Name the blood parasite species.
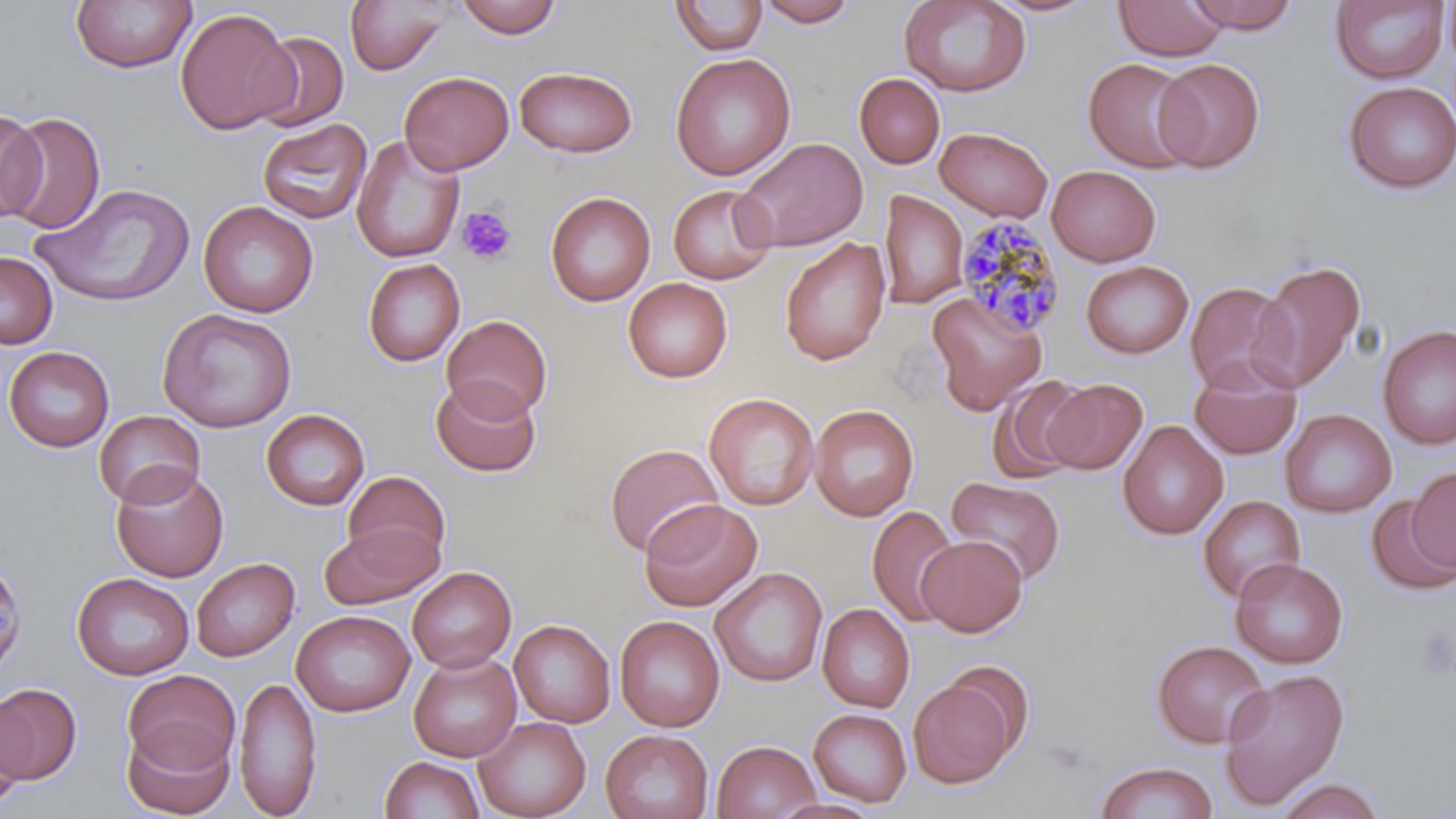

Plasmodium malariae.

preparation: thin blood film
uninfected_red_blood_cell_locations: 'approximate bounding boxes as [x1, y1, x2, y2] in pixels: [70, 0, 196, 74], [453, 0, 563, 39], [757, 0, 858, 27], [898, 0, 1032, 97], [987, 0, 1100, 17], [1184, 0, 1301, 33], [1443, 0, 1456, 68], [345, 1, 452, 76], [669, 1, 768, 56], [1113, 1, 1227, 61], [1329, 1, 1450, 85], [175, 8, 297, 135], [250, 31, 349, 132], [670, 52, 796, 181], [1082, 58, 1198, 173], [1153, 58, 1264, 173], [513, 65, 639, 157], [399, 70, 514, 174], [854, 74, 944, 168], [1342, 81, 1456, 194], [0, 110, 46, 223], [3, 111, 104, 234], [256, 117, 372, 224], [935, 127, 1053, 221], [350, 135, 466, 264], [734, 137, 869, 252], [1047, 165, 1161, 266], [32, 182, 194, 307], [667, 184, 776, 285], [879, 190, 968, 309], [544, 191, 656, 307], [198, 200, 319, 318], [779, 237, 891, 366], [0, 251, 58, 349], [1250, 258, 1367, 394], [362, 259, 465, 366], [1081, 260, 1194, 359], [623, 277, 733, 383], [1185, 281, 1295, 395], [927, 290, 1047, 414], [158, 307, 298, 432], [441, 314, 553, 422], [1377, 324, 1455, 451], [4, 346, 115, 452], [1188, 362, 1302, 460], [430, 377, 542, 477], [987, 377, 1091, 483], [1042, 378, 1147, 474], [703, 392, 820, 511], [808, 404, 920, 522], [261, 408, 371, 511], [1280, 409, 1396, 518], [93, 410, 206, 508], [1116, 420, 1228, 540], [604, 443, 724, 557], [109, 463, 229, 582], [1408, 467, 1456, 574], [342, 470, 451, 571], [947, 476, 1066, 586], [1197, 494, 1306, 603], [1365, 494, 1455, 595], [638, 499, 763, 612], [866, 505, 961, 628], [320, 523, 442, 610], [915, 535, 1027, 637], [0, 552, 28, 678], [191, 557, 299, 662], [1230, 558, 1349, 669], [407, 567, 517, 673], [710, 567, 828, 687], [71, 572, 195, 679], [817, 603, 916, 714], [291, 610, 415, 717], [614, 615, 725, 732], [509, 619, 615, 728], [1151, 640, 1270, 748], [408, 652, 522, 762], [943, 663, 1034, 755], [1218, 668, 1350, 809], [122, 669, 240, 775], [234, 675, 322, 818], [909, 679, 1016, 788], [0, 682, 82, 783], [0, 697, 34, 808], [808, 709, 912, 808], [473, 717, 592, 819], [121, 723, 234, 818], [600, 729, 714, 819], [712, 740, 821, 819], [379, 756, 485, 819], [1094, 761, 1218, 819], [1275, 777, 1386, 819], [772, 798, 883, 819]'
stain: May-Grünwald-Giemsa
platelet_locations: 'approximate bounding boxes as [x1, y1, x2, y2] in pixels: [456, 205, 518, 265], [1414, 627, 1455, 683]'
image_size: 1456×819 pixels
plasmodium_malariae_infected_red_blood_cell_locations: 'approximate bounding boxes as [x1, y1, x2, y2] in pixels: [953, 215, 1068, 337]'
field_of_view: one of a larger specimen
modality: optical microscopy
magnification: 1000x